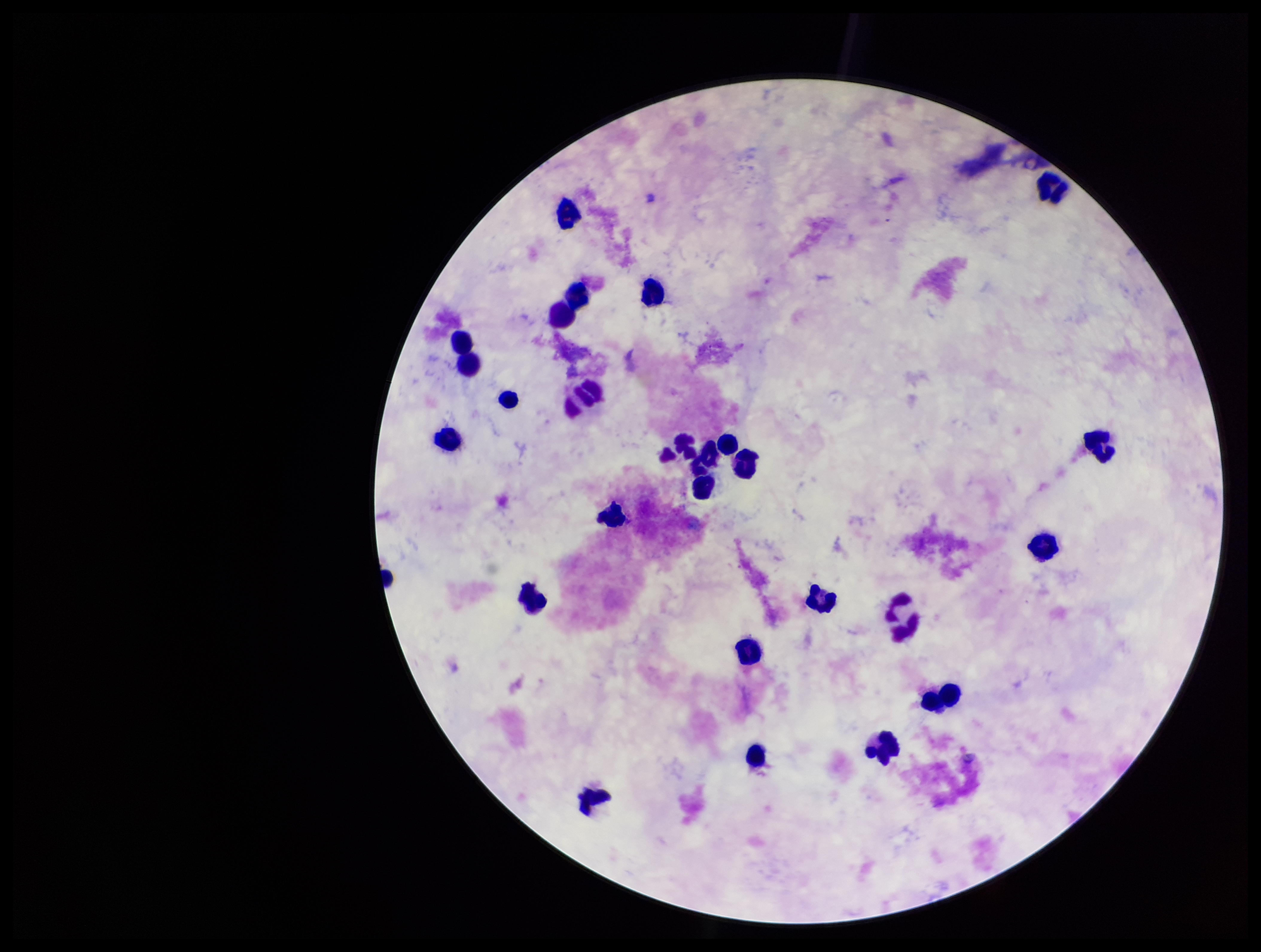

Summary:
  - Image size: 1261×952 pixels
  - Parasite count: 0
  - Leukocyte count: 24
  - Patient malaria status: negative
  - Stain: Giemsa
  - Field of view: one from this slide
  - Preparation: thick
  - Plasmodium parasites: none seen
  - Capture: smartphone photograph through the microscope eyepiece